Name the blood parasite species.
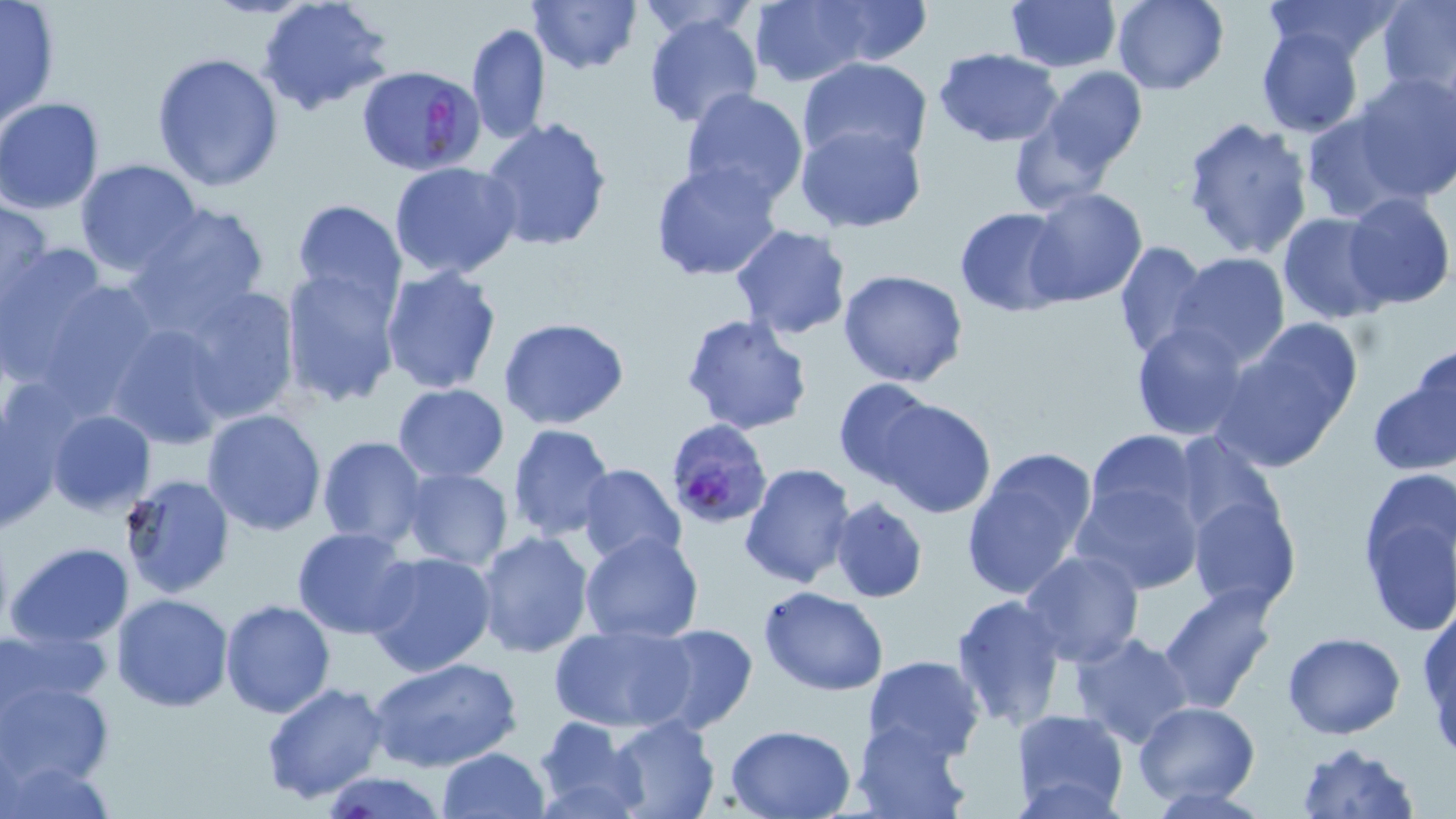
Plasmodium falciparum.

image_size: 1456×819 pixels
plasmodium_falciparum_infected_red_blood_cell_locations: 'approximate bounding boxes as (x1, y1, x2, y2) in pixels: (360, 67, 488, 180), (664, 423, 774, 535)'
uninfected_red_blood_cell_locations: 'approximate bounding boxes as (x1, y1, x2, y2) in pixels: (1, 0, 62, 128), (257, 0, 393, 115), (527, 0, 640, 73), (636, 0, 759, 40), (819, 0, 931, 65), (1110, 0, 1229, 94), (1260, 0, 1401, 66), (1005, 1, 1120, 73), (1378, 1, 1456, 99), (749, 2, 873, 86), (642, 13, 763, 129), (465, 22, 550, 146), (1253, 28, 1367, 137), (934, 48, 1062, 145), (151, 52, 285, 193), (798, 56, 932, 165), (1036, 67, 1148, 177), (1354, 71, 1456, 199), (680, 88, 809, 208), (0, 97, 105, 212), (1299, 111, 1417, 223), (480, 116, 613, 253), (1182, 116, 1314, 257), (795, 122, 928, 233), (75, 160, 203, 276), (648, 160, 783, 283), (389, 161, 521, 280), (1024, 188, 1149, 308), (1341, 193, 1455, 311), (0, 196, 51, 308), (293, 200, 406, 313), (126, 201, 270, 331), (954, 207, 1072, 316), (1277, 212, 1389, 323), (730, 224, 854, 339), (1113, 240, 1209, 361), (1, 244, 143, 407), (1170, 253, 1291, 372), (379, 264, 504, 394), (280, 270, 401, 406), (837, 270, 968, 389), (167, 281, 304, 427), (680, 313, 814, 434), (499, 317, 630, 429), (103, 319, 231, 449), (1130, 321, 1253, 441), (1212, 322, 1364, 473), (1410, 343, 1454, 457), (1366, 370, 1456, 478), (833, 377, 943, 487), (391, 383, 509, 483), (873, 395, 997, 519), (0, 397, 68, 532), (201, 408, 327, 536), (45, 409, 155, 517), (507, 423, 616, 540), (1086, 429, 1202, 531), (1171, 432, 1283, 552), (316, 436, 427, 551), (960, 446, 1099, 601), (738, 462, 856, 589), (576, 463, 686, 566), (399, 466, 513, 569), (1356, 469, 1455, 636), (119, 474, 235, 599), (1073, 480, 1202, 593), (1188, 489, 1302, 615), (829, 496, 927, 603), (292, 527, 415, 638), (475, 530, 594, 660), (580, 531, 704, 643), (6, 542, 133, 648), (1020, 550, 1144, 668), (363, 552, 497, 677), (1159, 584, 1279, 711), (759, 586, 890, 695), (112, 593, 235, 712), (950, 594, 1067, 730), (220, 599, 336, 718), (1419, 603, 1456, 745), (1082, 608, 1266, 729), (548, 622, 698, 733), (646, 623, 758, 736), (4, 624, 112, 710), (1071, 632, 1196, 749), (1281, 632, 1407, 739), (861, 655, 985, 766), (366, 656, 521, 773), (3, 679, 114, 787), (260, 681, 391, 805), (1132, 701, 1259, 804), (1011, 709, 1128, 816), (532, 714, 645, 818), (605, 714, 720, 818), (851, 718, 974, 819), (724, 723, 856, 817), (1294, 741, 1421, 819), (436, 747, 550, 819), (3, 754, 117, 819), (324, 771, 446, 818)'
stain: May-Grünwald-Giemsa
field_of_view: single
modality: light microscopy
preparation: thin blood smear
magnification: 1000x